Classify this cell by malaria status.
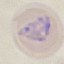

Parasitized.

capture: smartphone camera at the microscope eyepiece
stain: Giemsa
preparation: thin blood smear
image_type: cell patch, automatically extracted from a larger field of view and resized to 64 × 64 pixels